Assess the morphology of the red blood cells.
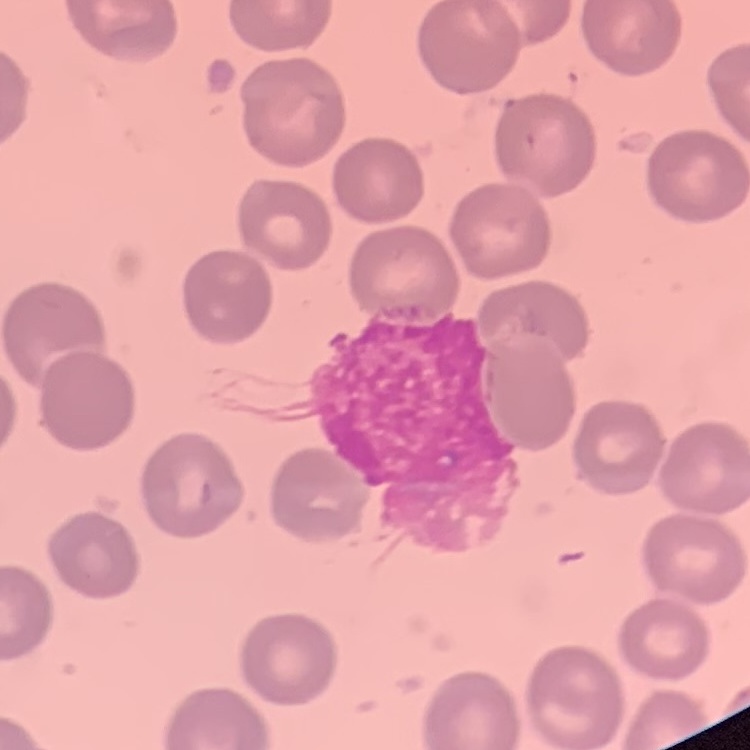

No rouleaux formation.

Field's or Giemsa stain. Thin peripheral smear. Square crop of a larger photomicrograph.